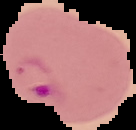 Segmented cell region on a black background. From a thin blood smear. Image is 136×130 pixels. Malaria status: parasitized.